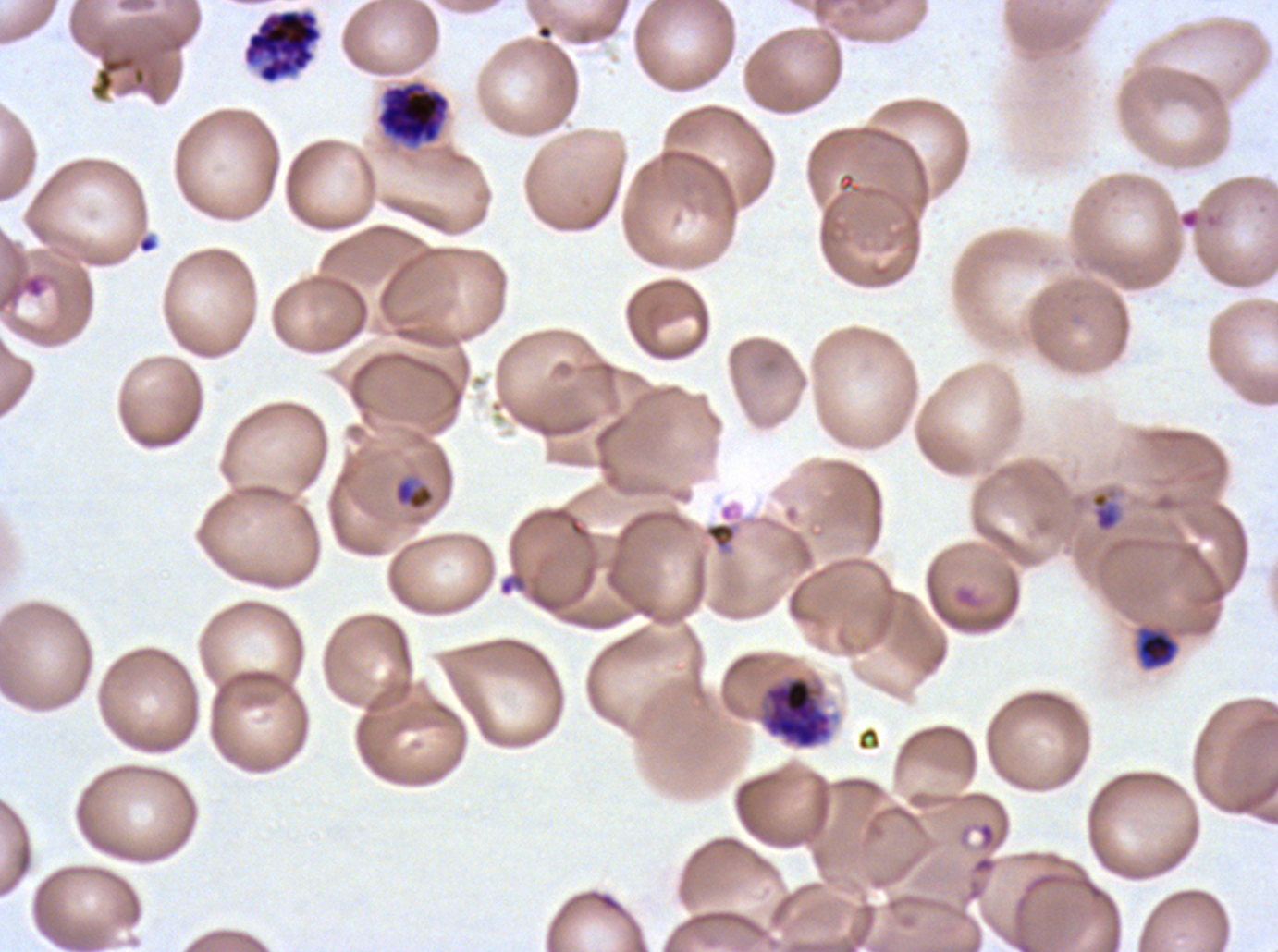 Approximate bounding rectangles given as corner coordinates in pixels from the top-left. Early schizont locations: (x1=756, y1=674, x2=834, y2=751). Ring locations: (x1=137, y1=234, x2=158, y2=254), (x1=22, y1=275, x2=45, y2=299), (x1=1091, y1=492, x2=1120, y2=531), (x1=498, y1=572, x2=527, y2=596). Late-ring/early-trophozoite locations: (x1=393, y1=476, x2=436, y2=511), (x1=1137, y1=629, x2=1178, y2=669). Segmenter locations: (x1=242, y1=8, x2=323, y2=84). Debris locations: (x1=90, y1=53, x2=147, y2=100). Late schizont locations: (x1=376, y1=81, x2=449, y2=145). Mid trophozoite locations: (x1=701, y1=501, x2=743, y2=558). Image is 1278×952 pixels. Ex-vivo Plasmodium falciparum culture from a patient in The Gambia, grown for 24 to 48 hours. Thin blood film. Life-cycle stages observed: ring, late-ring/early-trophozoite, mid trophozoite, early schizont, late schizont, segmenter. One sub-image of a larger composite. Giemsa stain.